Report the malaria status of this cell.
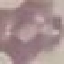

It is uninfected.

Acquired by smartphone through the microscope eyepiece. Giemsa stain. Cell patch, automatically extracted from a larger field of view and resized to 64 × 64 pixels. Thin smear of blood.